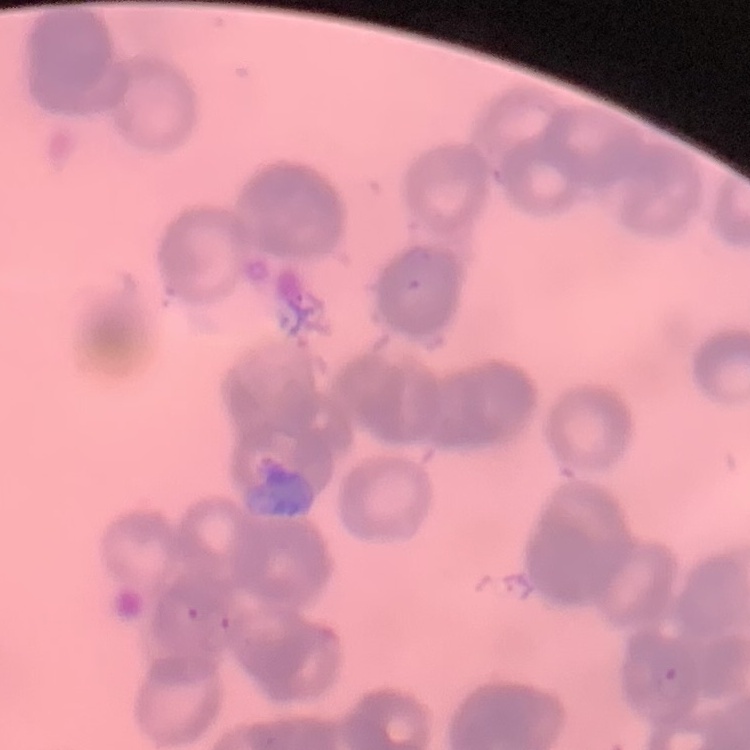

{
  "erythrocyte_morphology": "rouleaux formation",
  "stain": "Field's or Giemsa",
  "image_type": "square crop of a larger photomicrograph",
  "preparation": "thin peripheral smear"
}